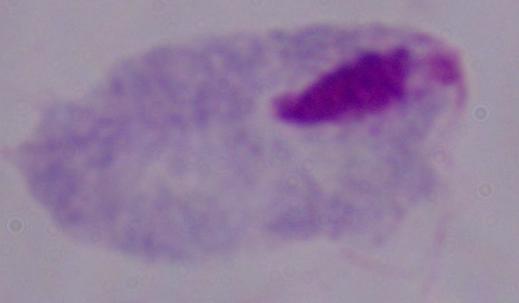 Captured at 1000x magnification. Photomicrograph. A trichomonad is shown.